Identify the preparation type.
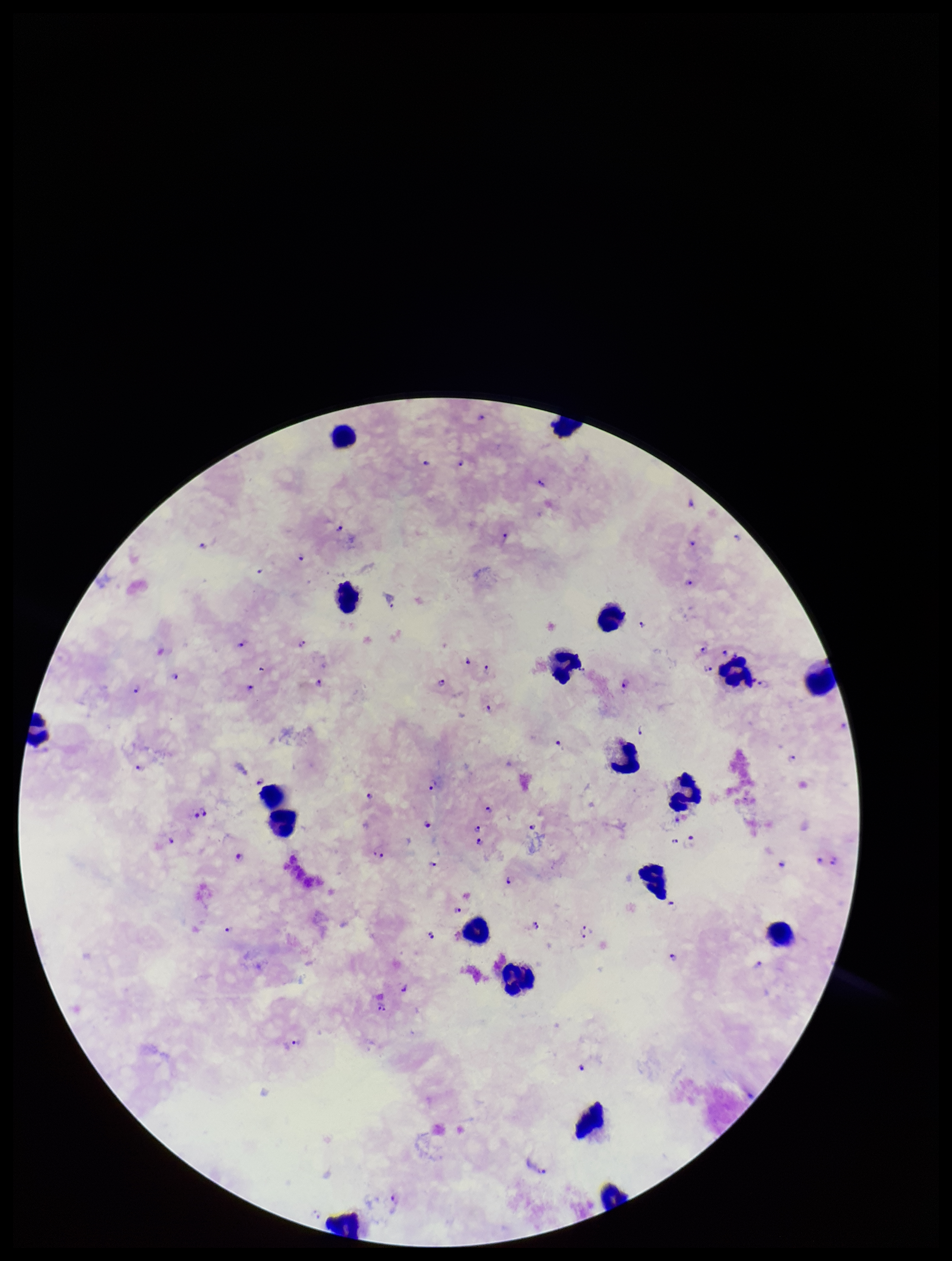
A thick smear.

Giemsa stain. Single field of view. Image is 952×1261 pixels. Smartphone photograph taken through the eyepiece of a microscope. Patient malaria status: infected. Plasmodium parasites: identified. Leukocyte count: 20. Parasite count: 78. Species reported for this patient: Plasmodium falciparum.